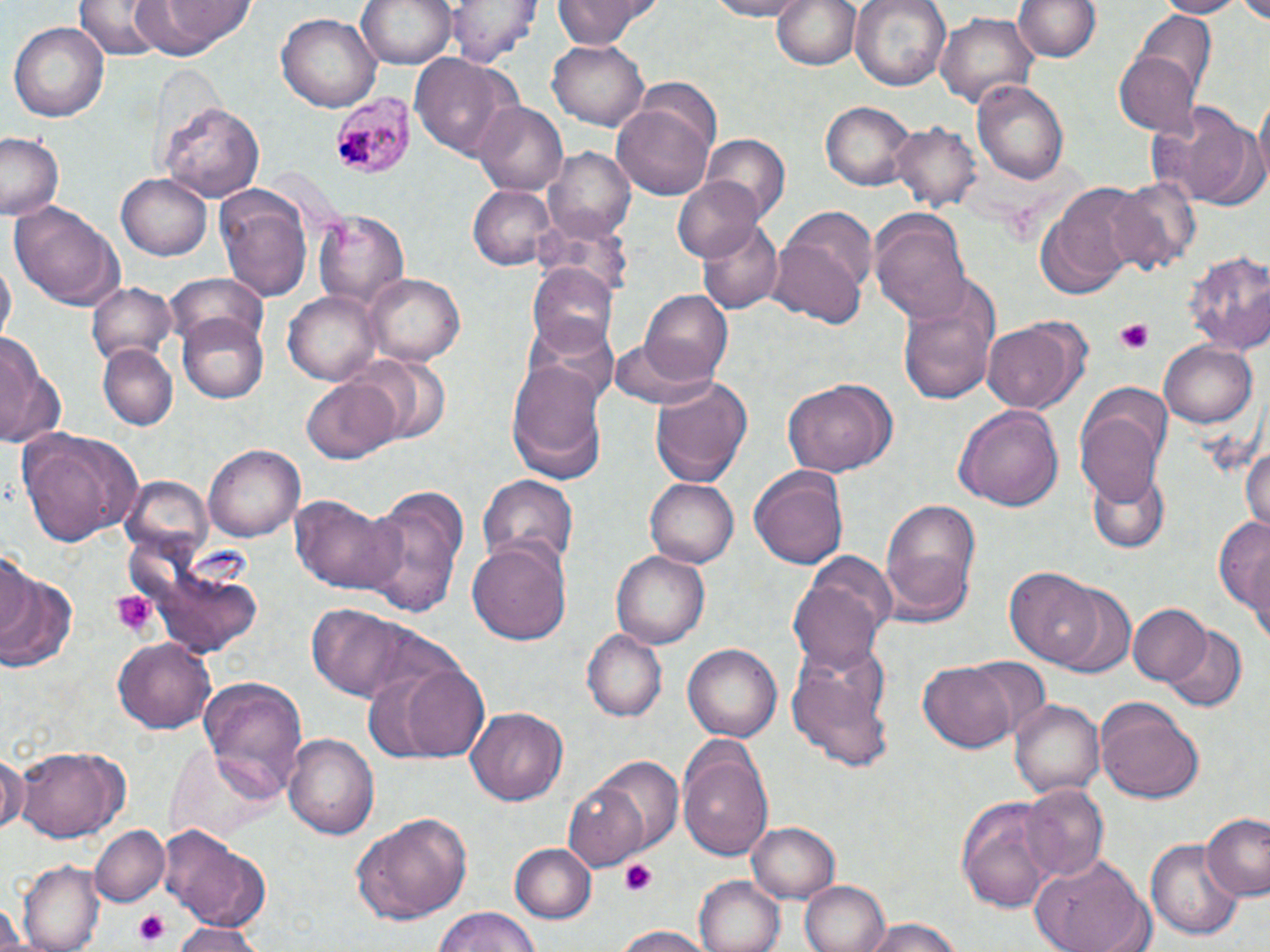
Summary:
  - Coordinate format: approximate bounding boxes as (x1, y1, x2, y2) in pixels
  - Platelet locations: (1114, 319, 1157, 354), (110, 589, 155, 639), (621, 859, 659, 898), (132, 909, 173, 947)
  - Plasmodium malariae-infected red blood cell locations: (332, 91, 417, 177)
  - Uninfected red blood cell locations: (132, 0, 257, 57), (356, 0, 458, 69), (448, 0, 540, 65), (551, 0, 658, 48), (700, 0, 811, 19), (850, 0, 950, 93), (1149, 0, 1250, 18), (774, 1, 861, 73), (1017, 1, 1099, 63), (1233, 1, 1270, 21), (75, 2, 165, 60), (937, 12, 1038, 109), (273, 13, 381, 112), (1135, 13, 1214, 95), (8, 21, 110, 122), (547, 37, 649, 130), (1113, 50, 1199, 137), (411, 52, 513, 162), (971, 79, 1070, 186), (1250, 93, 1270, 201), (820, 100, 915, 190), (161, 101, 264, 203), (1149, 101, 1255, 204), (475, 102, 568, 195), (613, 103, 716, 201), (890, 121, 979, 213), (0, 133, 65, 219), (703, 134, 789, 223), (546, 146, 635, 242), (118, 173, 211, 260), (673, 175, 764, 263), (1106, 175, 1200, 276), (1036, 181, 1144, 291), (468, 184, 555, 270), (218, 194, 312, 304), (12, 205, 125, 311), (783, 206, 878, 299), (313, 209, 411, 310), (870, 211, 973, 323), (697, 218, 783, 314), (768, 232, 870, 330), (1184, 253, 1270, 354), (529, 262, 621, 354), (165, 275, 268, 351), (364, 275, 465, 365), (898, 282, 1000, 409), (87, 284, 177, 369), (640, 289, 734, 386), (284, 292, 384, 384), (178, 311, 272, 403), (522, 315, 620, 408), (982, 318, 1087, 414), (0, 333, 54, 444), (611, 339, 712, 409), (1160, 341, 1257, 428), (98, 345, 176, 430), (349, 353, 453, 444), (507, 360, 611, 482), (649, 375, 754, 488), (303, 376, 401, 464), (782, 379, 896, 476), (955, 403, 1063, 515), (1075, 403, 1167, 507), (16, 427, 148, 549), (1242, 438, 1270, 534), (204, 444, 305, 542), (750, 466, 849, 573), (1089, 466, 1167, 553), (479, 474, 577, 573), (645, 475, 738, 566), (120, 476, 212, 562), (359, 483, 470, 618), (288, 493, 405, 597), (880, 497, 982, 618), (1214, 512, 1270, 637), (469, 536, 570, 647), (0, 550, 40, 650), (611, 550, 710, 648), (790, 552, 896, 675), (1006, 567, 1103, 667), (0, 568, 76, 676), (1054, 585, 1135, 674), (1127, 603, 1210, 688), (303, 604, 439, 705), (1164, 624, 1246, 711), (582, 629, 667, 723), (111, 638, 216, 735), (684, 642, 784, 741), (787, 647, 892, 771), (961, 654, 1053, 744), (370, 659, 491, 763), (920, 661, 1018, 751), (195, 678, 309, 797), (1010, 698, 1103, 798), (1096, 698, 1206, 804), (466, 707, 565, 806), (283, 733, 379, 840), (677, 744, 774, 862), (14, 746, 130, 841), (0, 748, 24, 836), (597, 758, 681, 848), (564, 781, 651, 869), (1024, 785, 1107, 881), (956, 796, 1061, 912), (1203, 811, 1270, 902), (354, 813, 468, 923), (748, 821, 842, 903), (91, 825, 169, 907), (160, 825, 270, 928), (1147, 839, 1244, 941), (508, 842, 595, 924), (1028, 854, 1153, 952), (17, 863, 103, 950), (694, 876, 784, 952), (801, 880, 889, 952), (2, 902, 36, 952), (430, 907, 542, 951), (860, 918, 971, 952), (168, 923, 263, 952), (611, 924, 716, 952)
  - Slide-level diagnosis: Plasmodium malariae
  - Stain: May-Grünwald-Giemsa
  - Modality: light microscopy
  - Magnification: 1000x
  - Image size: 1270×952 pixels
  - Field of view: single
  - Preparation: thin blood film